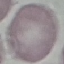

Summary:
  - Malaria status: uninfected
  - Image type: cell patch, automatically extracted from a larger field of view and resized to 64 × 64 pixels
  - Stain: Giemsa
  - Preparation: thin smear
  - Capture: smartphone through the microscope eyepiece